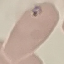

malaria_status: parasitized
image_type: cell patch, automatically extracted from a larger field of view and resized to 64 × 64 pixels
stain: Giemsa
preparation: thin smear
capture: smartphone camera at the microscope eyepiece